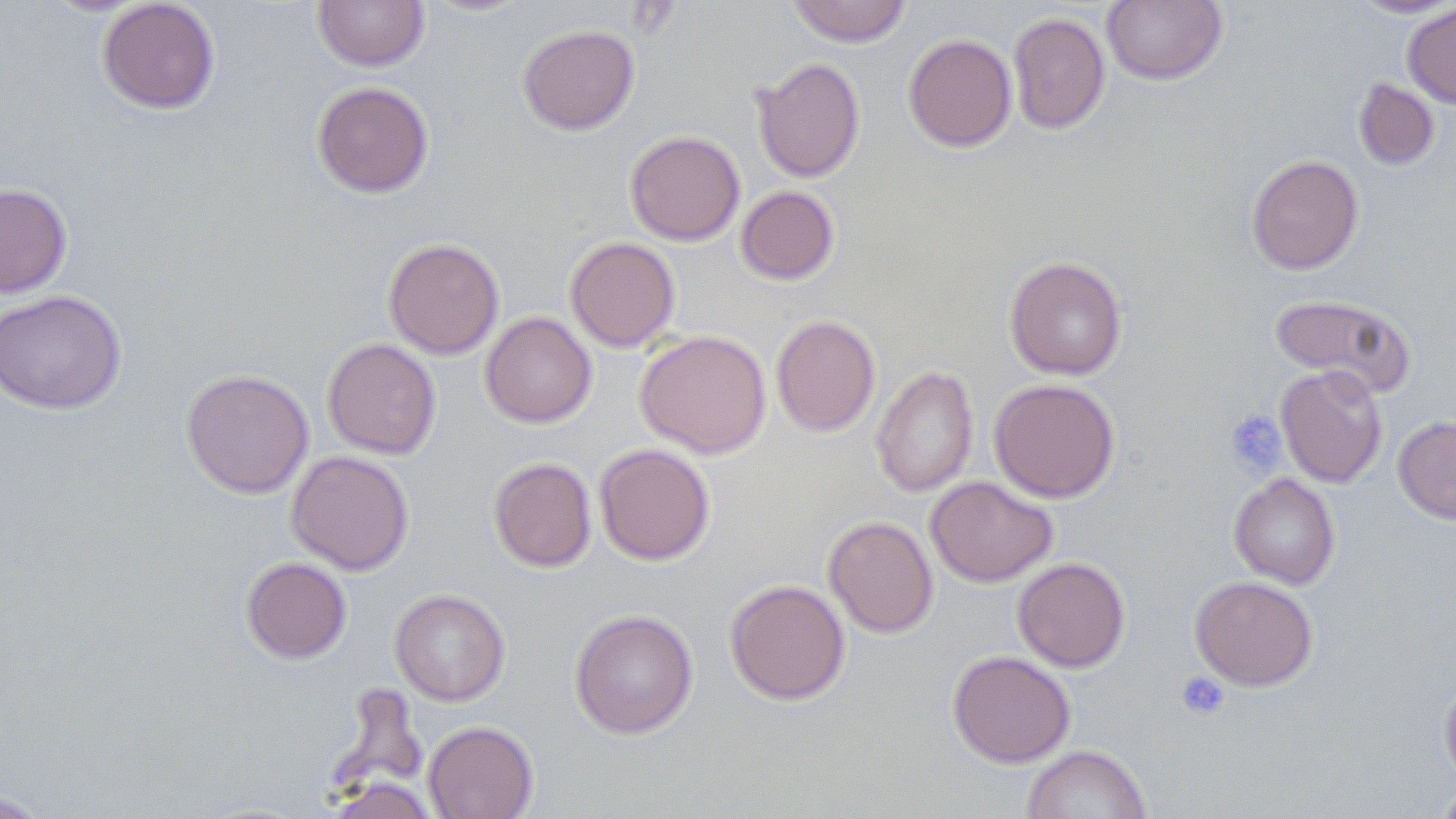

slide-level diagnosis = negative for blood parasites
preparation = thin blood film
platelet locations = approximate bounding boxes as (x1, y1, x2, y2) in pixels: (1224, 408, 1287, 477), (1175, 671, 1230, 722)
field of view = single
modality = optical microscopy
magnification = 1000x
image size = 1456×819 pixels
uninfected red blood cell locations = approximate bounding boxes as (x1, y1, x2, y2) in pixels: (97, 0, 221, 114), (313, 0, 430, 72), (420, 0, 535, 17), (788, 0, 912, 47), (1102, 0, 1227, 86), (1349, 0, 1456, 18), (1403, 3, 1456, 108), (1008, 12, 1110, 135), (517, 24, 639, 135), (903, 33, 1017, 152), (751, 57, 866, 183), (1353, 79, 1439, 171), (311, 81, 434, 198), (625, 131, 745, 245), (1246, 155, 1363, 275), (0, 183, 72, 297), (735, 185, 840, 285), (565, 236, 681, 352), (383, 238, 505, 359), (1004, 256, 1127, 380), (0, 290, 126, 414), (1268, 293, 1417, 397), (481, 312, 596, 427), (770, 315, 880, 437), (634, 330, 772, 459), (321, 338, 441, 460), (1276, 364, 1387, 488), (871, 365, 978, 498), (181, 369, 314, 499), (989, 378, 1120, 503), (1393, 415, 1456, 525), (594, 443, 715, 565), (286, 450, 415, 575), (489, 457, 596, 572), (1229, 473, 1340, 589), (925, 475, 1058, 587), (824, 516, 938, 638), (241, 557, 352, 664), (1013, 557, 1130, 672), (1190, 575, 1318, 691), (724, 579, 851, 705), (389, 588, 510, 706), (569, 608, 698, 739), (947, 650, 1076, 768), (1439, 674, 1456, 788), (325, 683, 429, 801), (423, 720, 539, 819), (1022, 744, 1152, 819), (325, 777, 438, 819), (1434, 780, 1456, 819), (1, 790, 51, 818)
stain = May-Grünwald-Giemsa